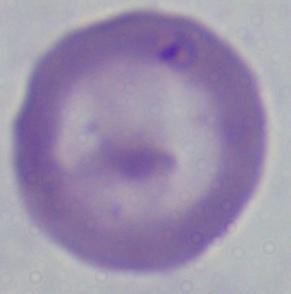

Summary:
  - Magnification: 1000x
  - Modality: photomicrograph
  - Identification: Babesia